Assess the morphology of the red blood cells.
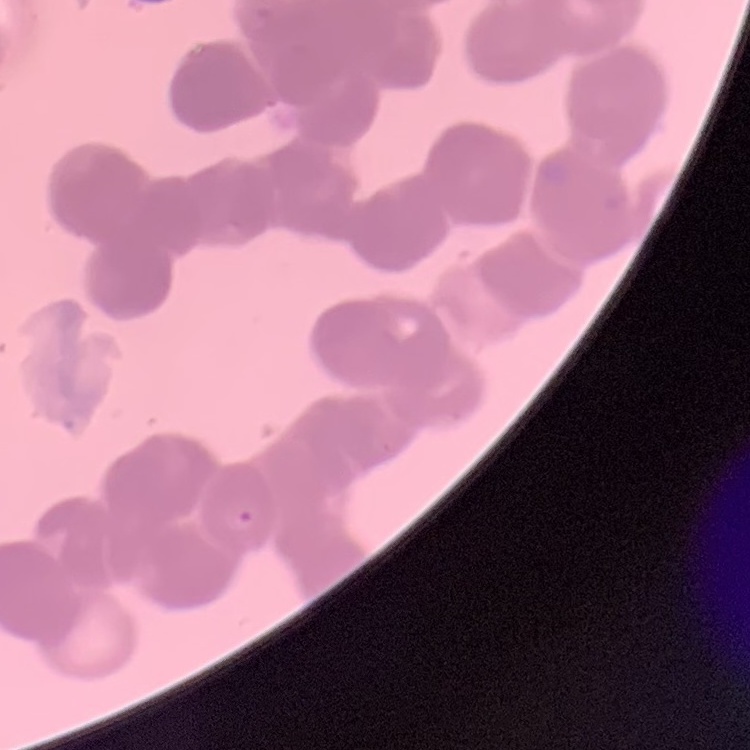

Rouleaux formation.

Summary:
  - Image type: square crop of a larger photomicrograph
  - Stain: Field's or Giemsa
  - Preparation: thin blood smear